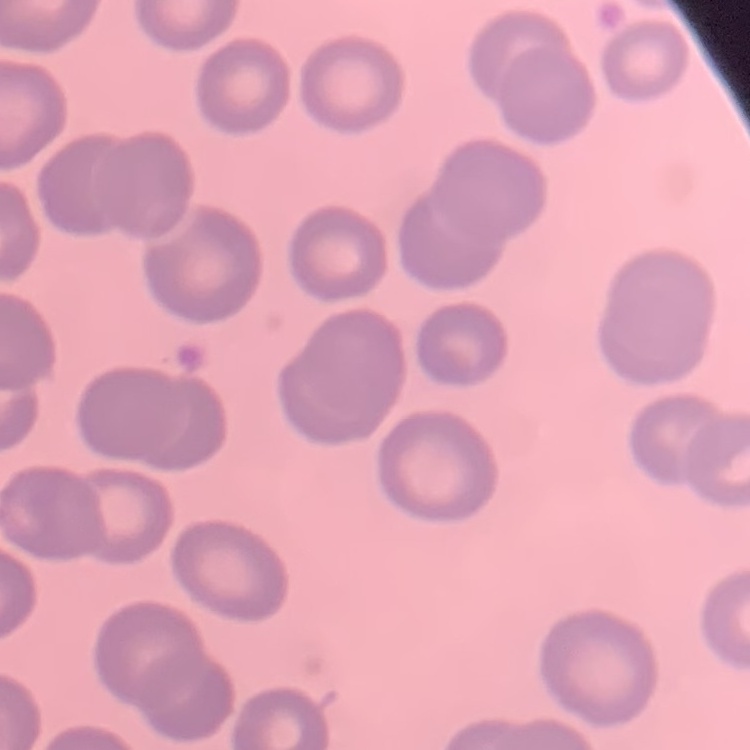

erythrocyte morphology = no rouleaux formation
stain = Field's or Giemsa
image type = one tile cut from a larger photomicrograph
preparation = thin blood smear